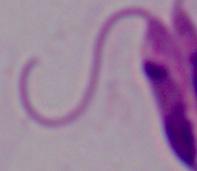 1000x magnification. Micrograph. A Leishmania parasite is shown.